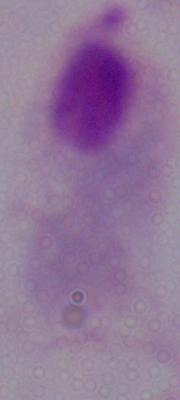
modality = photomicrograph
magnification = 1000x
identification = trichomonad